State which cell type is depicted.
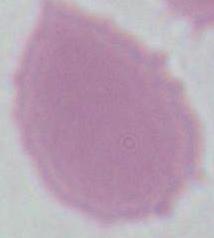

This is an erythrocyte.

Summary:
  - Magnification: 1000x
  - Modality: photomicrograph